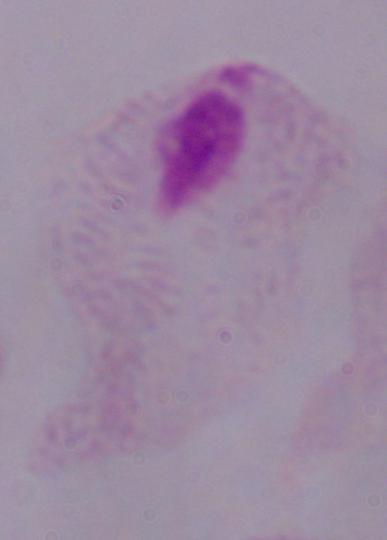
{
  "identification": "trichomonad",
  "modality": "photomicrograph",
  "magnification": "1000x"
}